Point out each Plasmodium parasite.
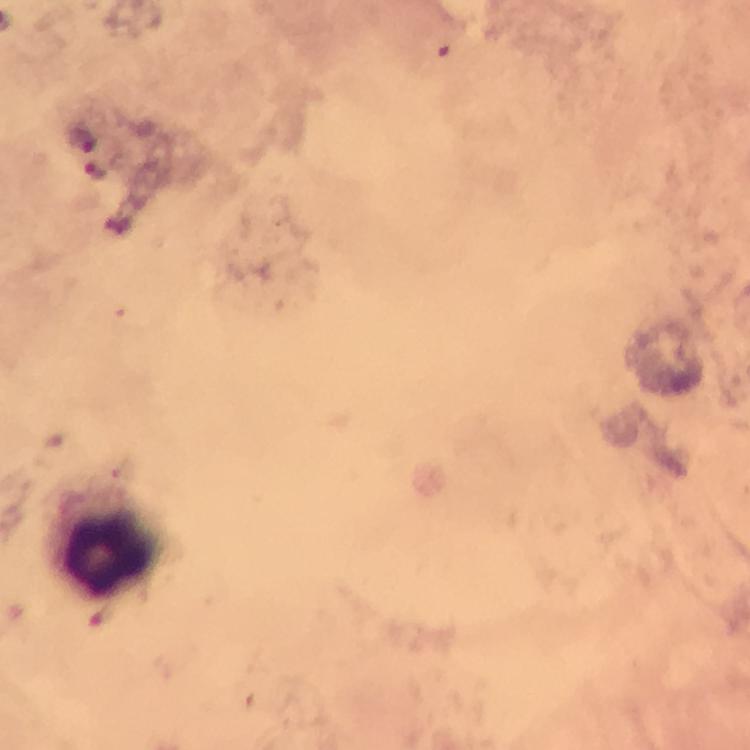
Approximate centers as (x, y) in pixels.
Plasmodium parasites: (96, 170).

Summary:
  - Leukocyte locations: (104, 545)
  - Magnification: 100x
  - Context: from a malaria diagnostic workup
  - Stain: Giemsa
  - Preparation: thick blood smear
  - Image size: 750×750 pixels
  - Cropped from: a single field of view
  - Capture: smartphone mounted on the microscope
  - Immersion oil: used